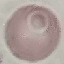

Summary:
  - Malaria status: uninfected
  - Capture: smartphone through the microscope eyepiece
  - Stain: Giemsa
  - Preparation: thin blood smear
  - Image type: automatically extracted cell patch, resized to 64 × 64 pixels